Give the extent of all uninfected red blood cells.
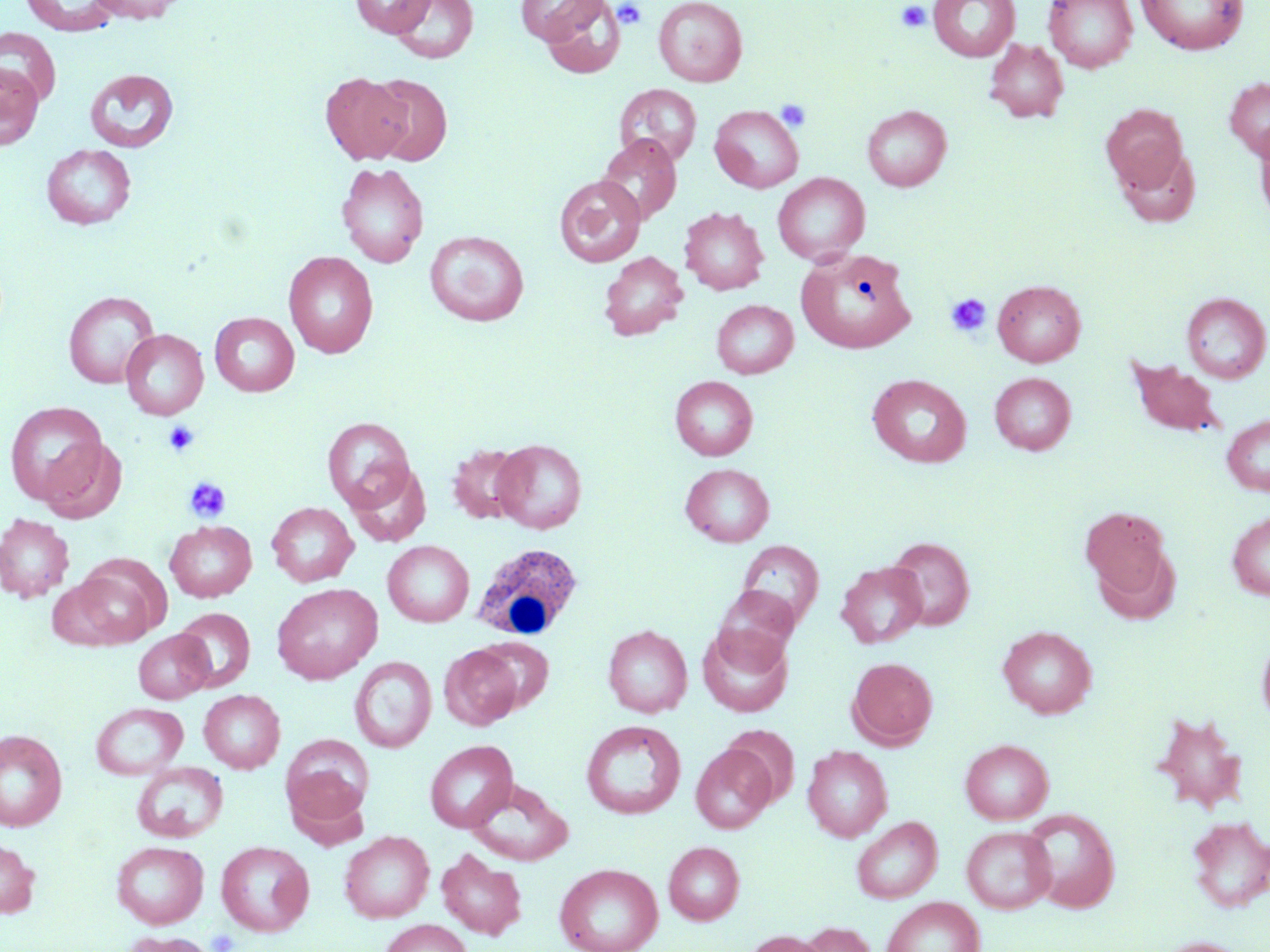
Approximate bounding boxes as [x1, y1, x2, y2] in pixels.
Uninfected red blood cells: [21, 0, 120, 35], [86, 0, 187, 23], [351, 0, 435, 37], [390, 0, 478, 64], [514, 0, 605, 44], [535, 0, 626, 79], [653, 0, 747, 87], [929, 0, 1019, 61], [1044, 0, 1137, 72], [1136, 0, 1248, 54], [0, 27, 60, 105], [985, 38, 1069, 123], [0, 62, 44, 150], [85, 69, 179, 152], [320, 72, 412, 164], [365, 73, 452, 165], [1224, 76, 1270, 161], [614, 84, 702, 166], [862, 104, 952, 192], [1101, 104, 1189, 193], [710, 105, 804, 193], [1253, 121, 1270, 225], [596, 133, 682, 224], [41, 143, 136, 230], [1114, 145, 1201, 228], [336, 162, 428, 268], [773, 173, 870, 265], [554, 175, 645, 267], [679, 206, 769, 295], [425, 230, 529, 326], [797, 248, 916, 353], [283, 251, 378, 358], [599, 251, 688, 340], [993, 279, 1086, 367], [63, 291, 159, 389], [1182, 292, 1270, 383], [711, 300, 797, 378], [210, 312, 299, 396], [121, 329, 208, 420], [1127, 357, 1226, 438], [989, 372, 1076, 455], [867, 374, 971, 467], [670, 376, 757, 460], [5, 401, 109, 506], [1222, 413, 1270, 495], [322, 417, 415, 511], [38, 436, 127, 524], [491, 439, 587, 533], [447, 443, 530, 524], [346, 463, 430, 546], [680, 463, 774, 547], [267, 502, 359, 587], [1079, 505, 1173, 605], [1226, 511, 1270, 601], [0, 514, 74, 602], [165, 520, 257, 602], [886, 535, 975, 630], [382, 540, 474, 627], [736, 540, 825, 631], [69, 561, 166, 647], [836, 561, 927, 648], [46, 578, 130, 651], [272, 583, 382, 684], [711, 586, 799, 670], [174, 607, 255, 691], [603, 624, 692, 718], [698, 624, 793, 717], [997, 626, 1097, 718], [133, 629, 214, 703], [1256, 632, 1270, 729], [475, 637, 553, 713], [440, 645, 523, 729], [349, 657, 436, 753], [848, 657, 937, 748], [199, 690, 285, 773], [91, 702, 188, 780], [1149, 711, 1248, 814], [581, 720, 685, 819], [0, 729, 68, 831], [282, 734, 373, 823], [960, 739, 1054, 824], [425, 740, 518, 832], [691, 744, 776, 833], [802, 745, 893, 842], [132, 762, 227, 843], [466, 780, 573, 867], [1021, 807, 1120, 912], [851, 816, 942, 903], [1186, 816, 1270, 913], [961, 827, 1056, 914], [339, 830, 434, 923], [0, 838, 39, 918], [216, 840, 314, 936], [111, 841, 208, 928], [664, 841, 745, 925], [436, 848, 527, 940], [555, 862, 663, 952], [881, 897, 985, 952], [379, 919, 473, 952], [799, 922, 877, 952], [119, 931, 216, 952], [742, 931, 832, 952], [1155, 937, 1252, 952].

Summary:
  - White blood cell locations: [471, 543, 583, 642]
  - Platelet locations: [612, 1, 647, 29], [896, 1, 931, 33], [776, 98, 811, 132], [945, 293, 992, 337], [162, 421, 199, 456], [185, 477, 232, 523]
  - Slide-level diagnosis: no evidence of blood parasites
  - Stain: May-Grünwald-Giemsa
  - Magnification: 1000x
  - Preparation: thin blood smear
  - Image size: 1270×952 pixels
  - Field of view: single
  - Modality: light microscopy